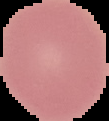
Image is 109×121 pixels. From a thin blood smear. Segmented cell region on a black background. Malaria status: uninfected.